Assess the morphology of the red blood cells.
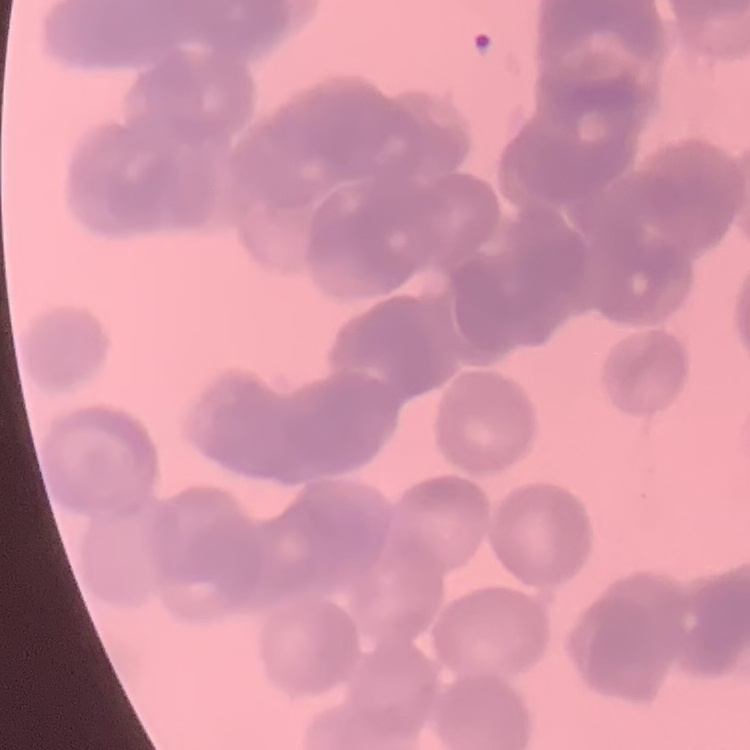

They show rouleaux formation.

Thin peripheral smear. Stained with either Field's or Giemsa. Square crop of a larger photomicrograph.